Identify the parasite.
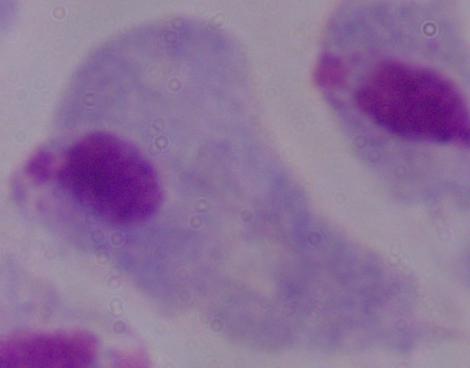

A trichomonad.

Summary:
  - Magnification: 1000x
  - Modality: photomicrograph